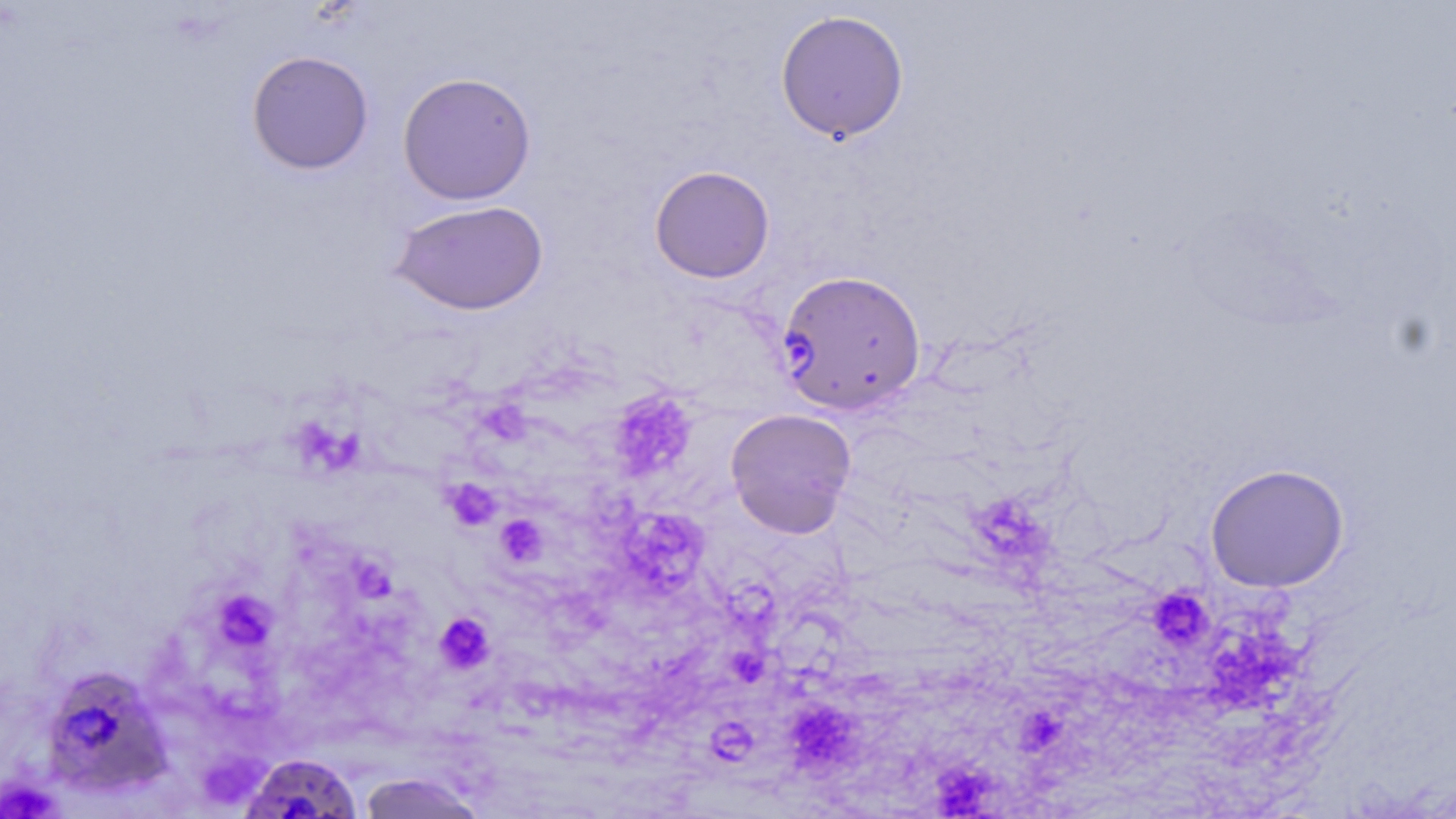
{
  "slide_level_diagnosis": "Plasmodium falciparum",
  "platelet_locations": "approximate bounding boxes as (x1,y1)-(x2,y2) corner pairs in pixels: (617,399)-(693,467), (488,403)-(531,447), (296,416)-(363,466), (444,479)-(501,531), (976,497)-(1042,554), (618,514)-(705,596), (496,515)-(547,565), (347,558)-(391,603), (1147,586)-(1214,651), (217,593)-(280,645), (435,611)-(495,674), (1216,621)-(1306,711), (733,651)-(763,682), (791,696)-(853,765), (1028,710)-(1063,745), (704,713)-(744,759), (936,765)-(996,819)",
  "modality": "optical microscopy",
  "plasmodium_falciparum_infected_red_blood_cell_locations": "approximate bounding boxes as (x1,y1)-(x2,y2) corner pairs in pixels: (777,269)-(927,415), (48,664)-(174,798), (239,753)-(363,819)",
  "preparation": "thin blood film",
  "field_of_view": "one of a larger specimen",
  "image_size": "1456×819 pixels",
  "uninfected_red_blood_cell_locations": "approximate bounding boxes as (x1,y1)-(x2,y2) corner pairs in pixels: (774,9)-(910,144), (246,50)-(374,175), (397,72)-(537,205), (649,165)-(775,283), (389,199)-(550,316), (725,408)-(857,538), (1205,463)-(1350,593), (356,772)-(490,819)",
  "stain": "May-Grünwald-Giemsa",
  "magnification": "1000x"
}